Report the malaria status.
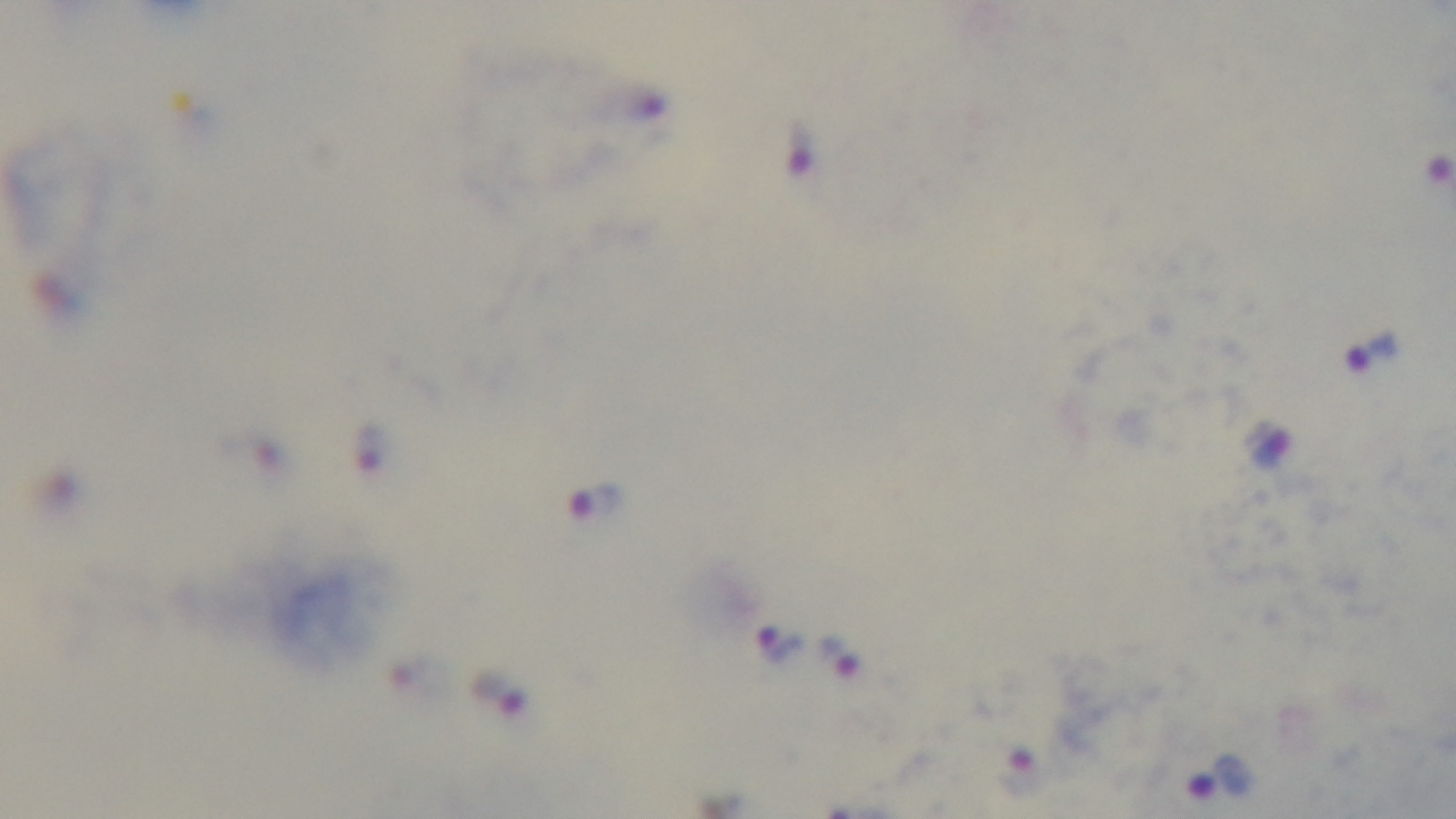

It is infected.

Summary:
  - Stain: Giemsa
  - Preparation: thick smear
  - Capture: mounted 4K digital camera
  - Field of view: single
  - Modality: light microscopy
  - Objective: 100x oil immersion